Outline each blood parasite and name the species.
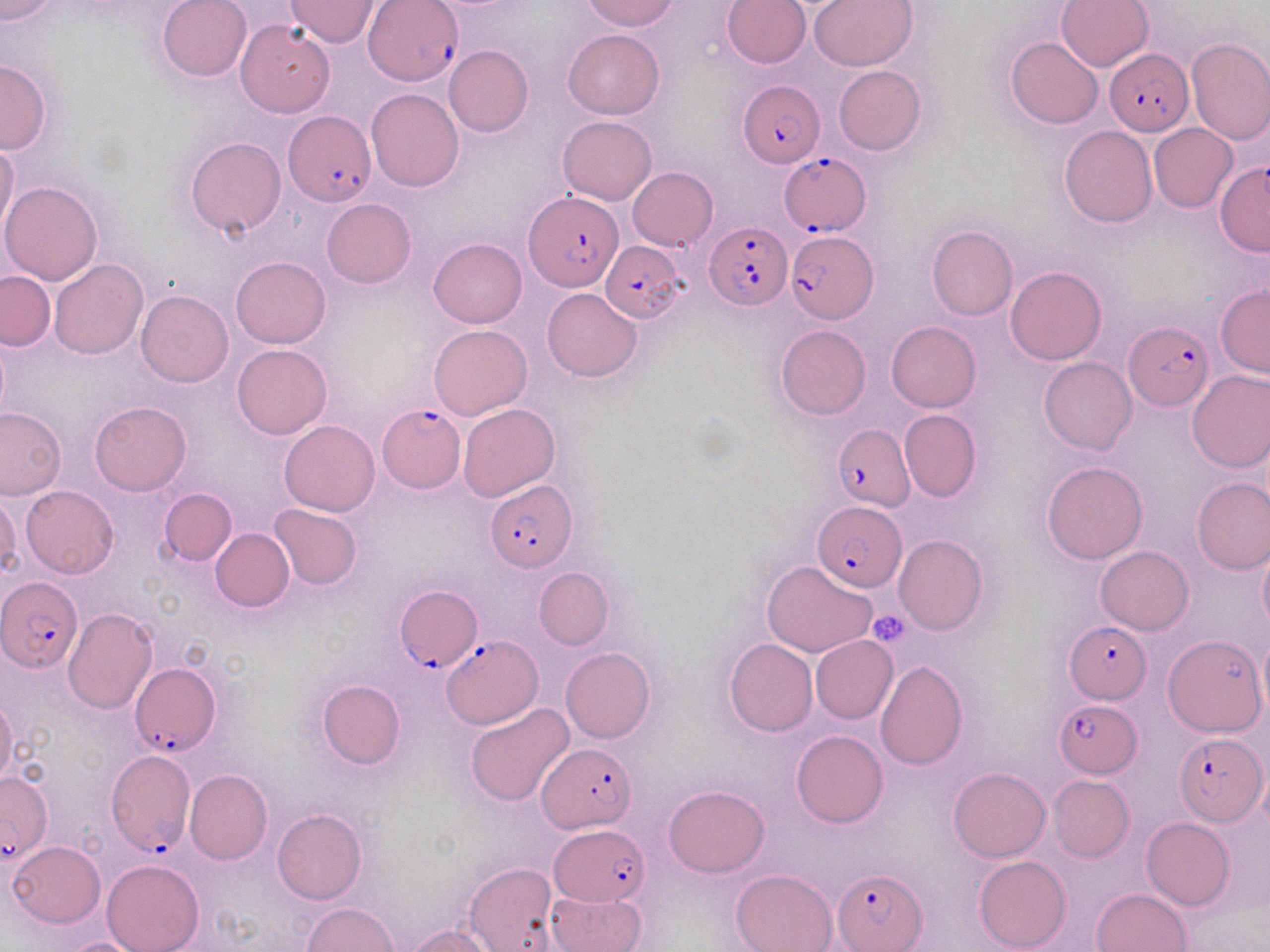

Approximate bounding boxes as named x1/y1/x2/y2 corners in pixels.
Plasmodium falciparum-infected red blood cells: (x1=366, y1=1, x2=466, y2=86), (x1=1105, y1=48, x2=1194, y2=136), (x1=737, y1=77, x2=824, y2=165), (x1=283, y1=110, x2=377, y2=207), (x1=780, y1=154, x2=872, y2=235), (x1=1215, y1=162, x2=1270, y2=257), (x1=523, y1=191, x2=622, y2=294), (x1=705, y1=222, x2=789, y2=311), (x1=785, y1=231, x2=878, y2=324), (x1=601, y1=239, x2=687, y2=325), (x1=1124, y1=322, x2=1212, y2=408), (x1=378, y1=404, x2=464, y2=493), (x1=834, y1=424, x2=914, y2=511), (x1=485, y1=481, x2=577, y2=571), (x1=814, y1=502, x2=907, y2=590), (x1=2, y1=577, x2=83, y2=671), (x1=394, y1=586, x2=479, y2=672), (x1=1064, y1=620, x2=1153, y2=703), (x1=442, y1=635, x2=541, y2=728), (x1=130, y1=662, x2=221, y2=756), (x1=1054, y1=699, x2=1142, y2=776), (x1=1173, y1=732, x2=1268, y2=825), (x1=538, y1=743, x2=639, y2=832), (x1=105, y1=752, x2=194, y2=857), (x1=0, y1=770, x2=54, y2=865), (x1=550, y1=825, x2=650, y2=905), (x1=834, y1=868, x2=927, y2=951).
No Plasmodium ovale, Plasmodium malariae, Plasmodium vivax, Babesia divergens, or Trypanosoma brucei observed.

Summary:
  - Uninfected red blood cell locations: (x1=0, y1=0, x2=59, y2=24), (x1=156, y1=0, x2=251, y2=83), (x1=582, y1=0, x2=680, y2=31), (x1=722, y1=0, x2=809, y2=69), (x1=807, y1=0, x2=919, y2=71), (x1=1056, y1=0, x2=1154, y2=71), (x1=284, y1=1, x2=380, y2=47), (x1=236, y1=20, x2=335, y2=117), (x1=563, y1=28, x2=664, y2=120), (x1=1005, y1=37, x2=1103, y2=129), (x1=1185, y1=37, x2=1270, y2=145), (x1=443, y1=45, x2=533, y2=137), (x1=0, y1=58, x2=51, y2=154), (x1=833, y1=66, x2=925, y2=155), (x1=367, y1=87, x2=464, y2=191), (x1=558, y1=116, x2=656, y2=206), (x1=1149, y1=123, x2=1238, y2=213), (x1=1059, y1=125, x2=1157, y2=228), (x1=184, y1=137, x2=285, y2=238), (x1=0, y1=140, x2=19, y2=239), (x1=628, y1=167, x2=717, y2=250), (x1=0, y1=181, x2=104, y2=284), (x1=321, y1=199, x2=417, y2=288), (x1=926, y1=224, x2=1017, y2=321), (x1=429, y1=237, x2=527, y2=328), (x1=231, y1=256, x2=330, y2=348), (x1=49, y1=259, x2=148, y2=359), (x1=1005, y1=266, x2=1107, y2=364), (x1=1, y1=271, x2=54, y2=350), (x1=1216, y1=283, x2=1270, y2=377), (x1=542, y1=287, x2=642, y2=382), (x1=137, y1=290, x2=234, y2=387), (x1=886, y1=321, x2=981, y2=412), (x1=429, y1=325, x2=532, y2=421), (x1=775, y1=325, x2=871, y2=420), (x1=231, y1=344, x2=332, y2=439), (x1=1038, y1=357, x2=1136, y2=454), (x1=1186, y1=370, x2=1270, y2=472), (x1=90, y1=400, x2=192, y2=495), (x1=458, y1=404, x2=560, y2=503), (x1=0, y1=406, x2=66, y2=500), (x1=899, y1=409, x2=982, y2=502), (x1=280, y1=420, x2=379, y2=517), (x1=1041, y1=460, x2=1149, y2=565), (x1=1192, y1=478, x2=1270, y2=574), (x1=20, y1=485, x2=119, y2=578), (x1=159, y1=488, x2=236, y2=566), (x1=0, y1=493, x2=21, y2=580), (x1=268, y1=504, x2=362, y2=590), (x1=211, y1=528, x2=294, y2=612), (x1=893, y1=534, x2=988, y2=635), (x1=1257, y1=541, x2=1270, y2=633), (x1=1096, y1=546, x2=1193, y2=635), (x1=762, y1=559, x2=877, y2=657), (x1=534, y1=567, x2=614, y2=650), (x1=63, y1=609, x2=158, y2=714), (x1=1257, y1=631, x2=1269, y2=717), (x1=811, y1=634, x2=897, y2=723), (x1=1162, y1=634, x2=1266, y2=738), (x1=724, y1=639, x2=818, y2=736), (x1=560, y1=647, x2=655, y2=743), (x1=874, y1=660, x2=968, y2=770), (x1=316, y1=680, x2=405, y2=770), (x1=0, y1=696, x2=19, y2=790), (x1=464, y1=703, x2=574, y2=807), (x1=792, y1=730, x2=888, y2=828), (x1=948, y1=767, x2=1051, y2=862), (x1=185, y1=770, x2=272, y2=864), (x1=1048, y1=775, x2=1133, y2=861), (x1=664, y1=784, x2=769, y2=877), (x1=271, y1=808, x2=367, y2=905), (x1=1141, y1=817, x2=1234, y2=910), (x1=8, y1=840, x2=106, y2=928), (x1=973, y1=855, x2=1070, y2=951), (x1=102, y1=859, x2=204, y2=952), (x1=464, y1=863, x2=558, y2=951), (x1=730, y1=867, x2=838, y2=952), (x1=1092, y1=888, x2=1190, y2=951), (x1=545, y1=890, x2=646, y2=952), (x1=300, y1=903, x2=399, y2=952), (x1=406, y1=924, x2=497, y2=951), (x1=58, y1=937, x2=153, y2=952)
  - Platelet locations: (x1=868, y1=609, x2=912, y2=647)
  - Slide-level diagnosis: Plasmodium falciparum
  - Field of view: one of a larger specimen
  - Modality: optical microscopy
  - Image size: 1270×952 pixels
  - Stain: May-Grünwald-Giemsa
  - Magnification: 1000x
  - Preparation: thin blood film